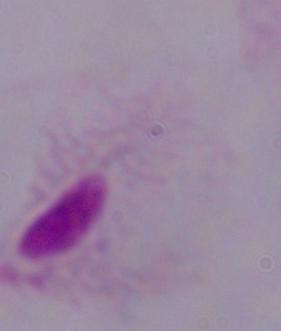
magnification = 1000x
modality = photomicrograph
identification = trichomonad